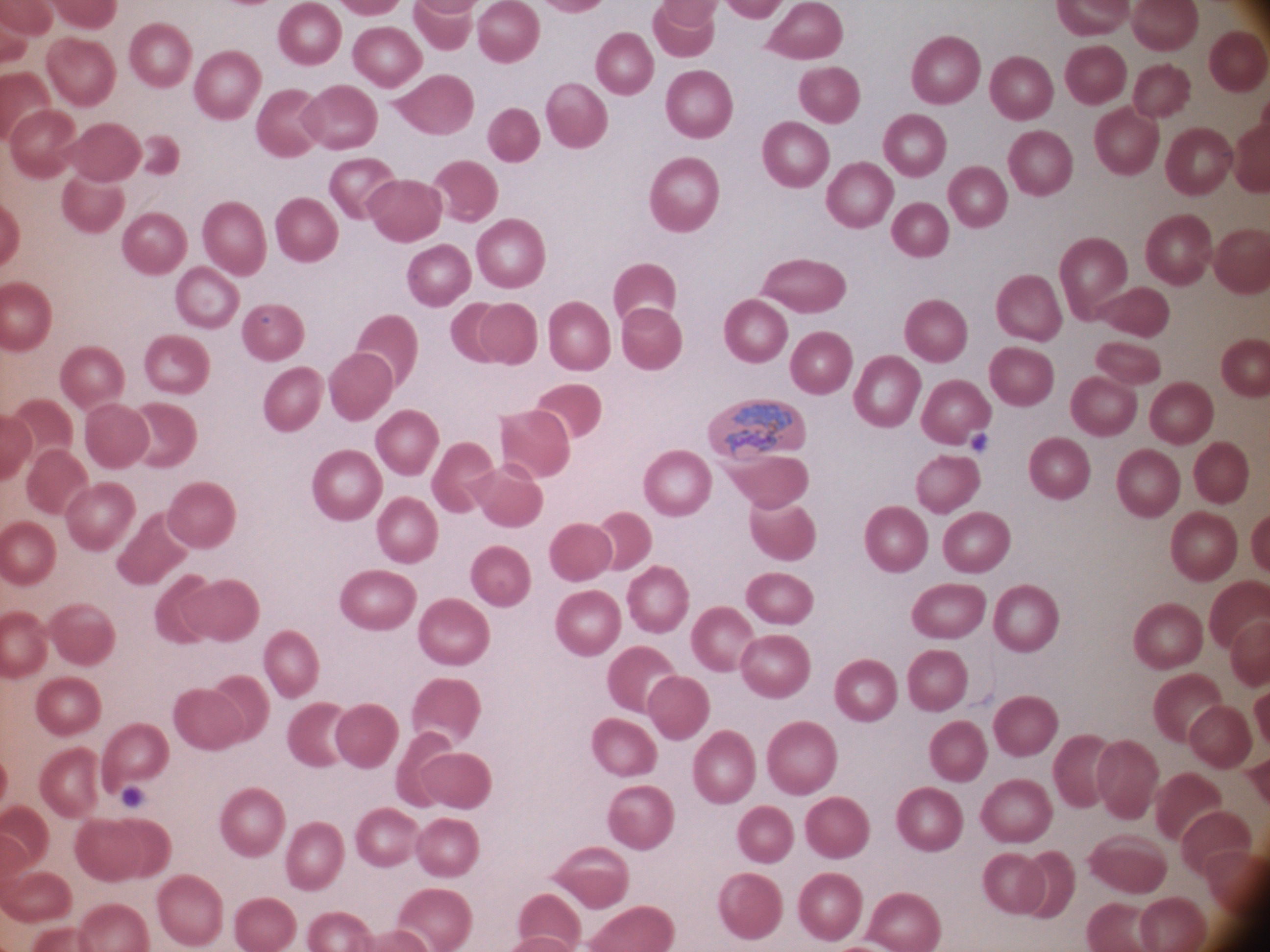

stain: Giemsa
trophozoite_locations: 'approximate bounding boxes as (x1, y1, x2, y2) in pixels, from the source annotation, which is not necessarily exhaustive: (725, 401, 792, 456)'
magnification: 100x
microscope: Leica DM2000 with built-in camera
image_size: 1270×952 pixels
field_of_view: one from this slide
preparation: thin blood smear
species: Plasmodium ovale